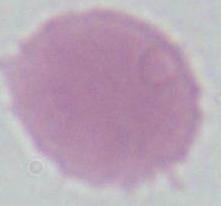
magnification: 1000x
identification: red blood cell
modality: micrograph